Give the position of every Plasmodium parasite visible.
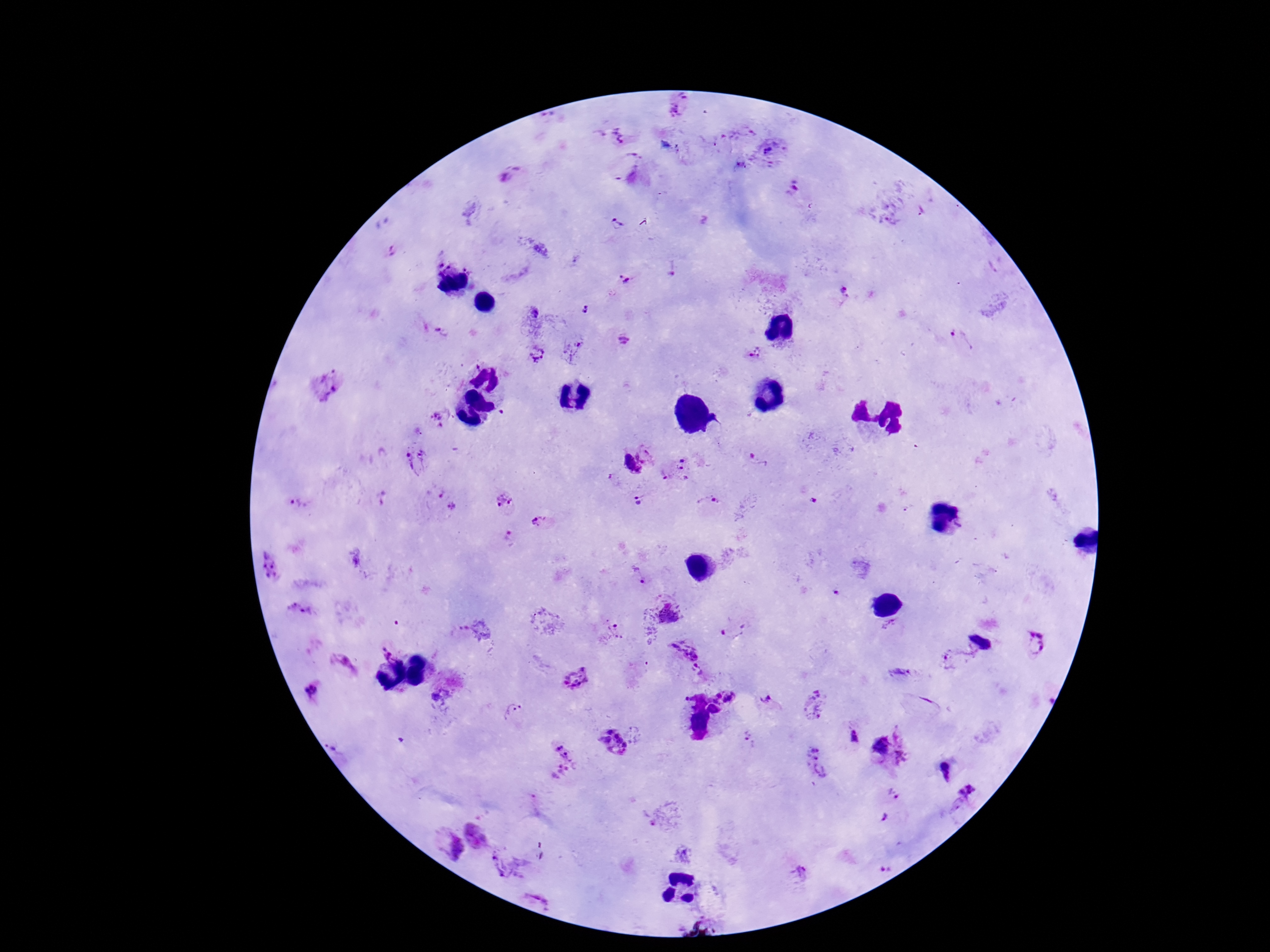
Approximate centers as (x, y) in pixels.
Plasmodium parasites: (680, 104), (613, 137), (770, 149), (741, 166), (510, 174), (793, 188), (924, 212), (888, 218), (619, 222), (621, 280), (846, 292), (585, 309), (533, 312), (624, 340), (960, 340), (571, 349), (535, 354), (757, 354), (438, 420), (648, 452), (416, 459), (759, 459), (630, 466), (676, 469), (436, 491), (504, 500), (637, 500), (297, 504), (709, 506), (451, 507), (540, 521), (510, 538), (357, 556), (271, 566), (638, 578), (300, 609), (668, 614), (735, 627), (891, 627), (461, 630), (609, 632), (1035, 642), (382, 643), (684, 648), (955, 657), (346, 665), (701, 668), (897, 672), (577, 678), (313, 691), (730, 697), (442, 700), (769, 700), (814, 704), (514, 711), (851, 737), (748, 739), (613, 741), (908, 742), (880, 748), (557, 763), (814, 763), (944, 769), (966, 791), (894, 794), (882, 818), (475, 836), (446, 843), (506, 862), (884, 868), (799, 872), (539, 893).

100x magnification. Patient malaria status: infected. Thick blood film. Image is 1270×952 pixels. Giemsa stain. Single field of view. Photographed through the microscope eyepiece with a smartphone camera.